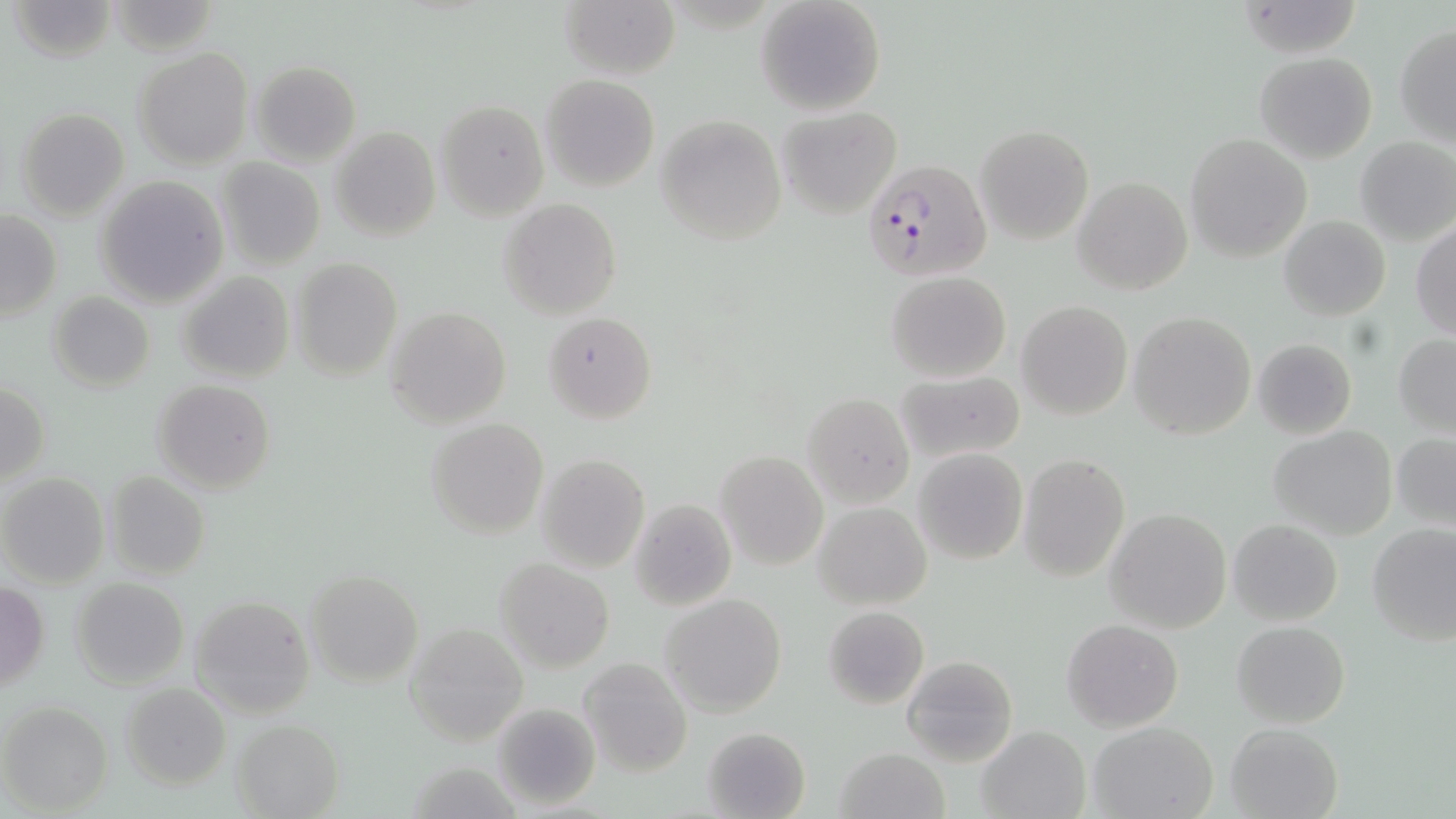 Approximate bounding boxes as [x1, y1, x2, y2] in pixels. Uninfected red blood cell locations: [559, 0, 681, 80], [756, 0, 887, 117], [9, 1, 117, 62], [1234, 2, 1362, 57], [1395, 24, 1456, 145], [133, 46, 253, 169], [1255, 51, 1379, 164], [249, 60, 361, 166], [541, 73, 659, 191], [435, 99, 547, 220], [778, 106, 902, 219], [15, 108, 130, 221], [655, 115, 787, 245], [975, 125, 1094, 245], [330, 126, 441, 243], [1185, 133, 1312, 261], [1354, 136, 1456, 246], [217, 157, 324, 269], [95, 176, 227, 307], [1073, 176, 1192, 296], [498, 198, 622, 319], [0, 210, 62, 322], [1279, 215, 1390, 320], [1411, 219, 1456, 342], [291, 257, 401, 380], [176, 271, 294, 384], [886, 272, 1011, 383], [48, 290, 155, 393], [1016, 301, 1133, 420], [384, 307, 512, 428], [543, 310, 657, 425], [1128, 311, 1257, 441], [1392, 334, 1455, 435], [1252, 338, 1357, 439], [894, 370, 1026, 463], [1, 380, 50, 488], [152, 380, 276, 495], [802, 394, 913, 507], [729, 410, 866, 550], [425, 419, 548, 537], [1268, 425, 1398, 539], [1391, 431, 1456, 530], [913, 448, 1027, 564], [717, 450, 828, 569], [536, 454, 649, 571], [1019, 454, 1130, 582], [104, 471, 211, 581], [0, 473, 111, 588], [628, 498, 737, 611], [811, 501, 933, 609], [1105, 507, 1233, 632], [1227, 518, 1343, 625], [1365, 524, 1456, 645], [494, 556, 616, 674], [305, 567, 425, 688], [70, 577, 189, 688], [0, 580, 48, 691], [659, 593, 788, 718], [190, 596, 316, 717], [822, 605, 931, 711], [1062, 619, 1183, 731], [1232, 620, 1350, 729], [403, 624, 528, 747], [902, 654, 1016, 766], [581, 656, 692, 777], [120, 683, 232, 790], [1, 700, 112, 813], [491, 702, 600, 811], [231, 720, 343, 818], [1088, 721, 1218, 817], [1224, 721, 1345, 819], [701, 726, 812, 819], [976, 726, 1089, 818], [834, 746, 950, 819]. Plasmodium falciparum-infected red blood cell locations: [862, 159, 999, 287]. Slide-level diagnosis: Plasmodium falciparum. Optical microscopy. Thin blood film. May-Grünwald-Giemsa-stained preparation. 1000x magnification. Image is 1456×819 pixels. Single field of view.